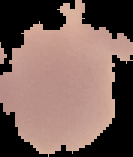 Image is 133×157 pixels. From a thin blood film. Malaria status: uninfected. Segmented cell region on a black background.